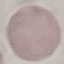 Result: negative for malaria parasites. Thin smear of blood. Giemsa stain. Automatically extracted cell patch, resized to 64 × 64 pixels. Acquired by smartphone through the microscope eyepiece.